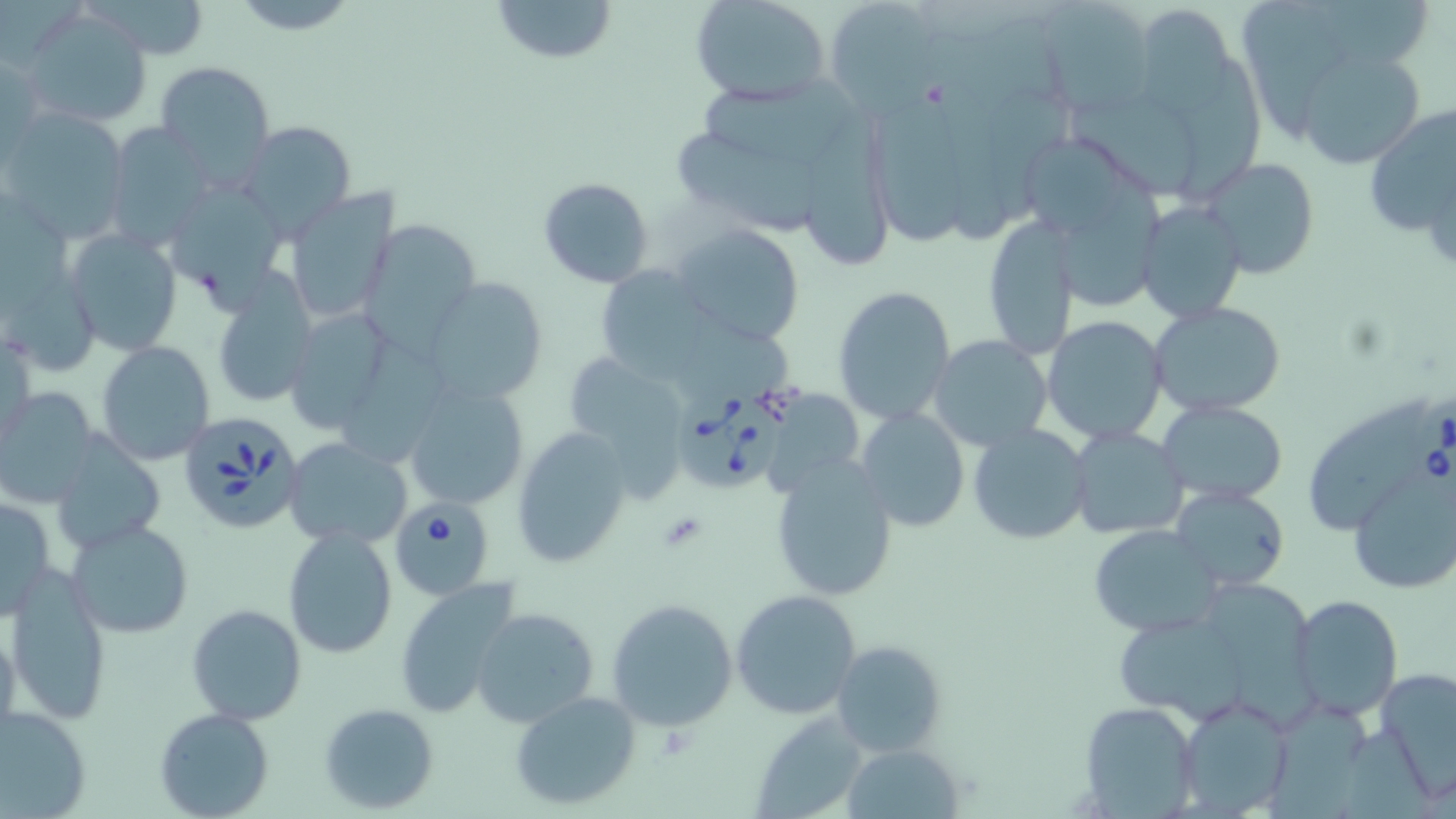

slide-level diagnosis = Babesia divergens
uninfected red blood cell locations = approximate bounding boxes as (x1,y1)-(x2,y2) corner pairs in pixels: (227,0)-(362,34), (490,0)-(619,65), (689,0)-(833,107), (823,0)-(947,114), (1036,0)-(1157,116), (1240,1)-(1365,145), (22,8)-(154,127), (1145,13)-(1235,123), (1296,47)-(1427,169), (1174,55)-(1270,209), (157,62)-(274,180), (704,75)-(859,159), (1071,96)-(1207,194), (873,99)-(972,252), (807,105)-(897,265), (1361,106)-(1456,242), (1,111)-(130,243), (238,121)-(356,237), (102,124)-(216,245), (673,127)-(811,231), (1197,157)-(1323,280), (1056,171)-(1166,305), (537,176)-(655,288), (175,186)-(287,311), (283,188)-(400,325), (1135,199)-(1247,323), (981,214)-(1082,360), (360,217)-(479,348), (670,222)-(807,345), (65,230)-(181,353), (597,267)-(720,386), (422,276)-(549,409), (211,282)-(319,410), (832,285)-(956,424), (1149,302)-(1288,419), (280,305)-(402,437), (1041,315)-(1169,444), (682,319)-(799,394), (928,335)-(1055,454), (352,338)-(447,464), (96,341)-(214,465), (576,358)-(698,501), (401,384)-(531,513), (0,387)-(99,509), (1157,399)-(1287,505), (1307,399)-(1434,535), (858,406)-(970,531), (967,422)-(1093,547), (511,426)-(630,568), (1068,427)-(1189,541), (49,434)-(166,556), (284,437)-(413,550), (768,455)-(899,599), (1345,466)-(1455,593), (1170,485)-(1290,592), (1,495)-(54,619), (67,519)-(194,638), (282,525)-(398,660), (1089,525)-(1224,635), (4,568)-(112,724), (394,577)-(522,719), (1215,579)-(1334,731), (730,589)-(862,719), (1287,594)-(1403,721), (607,598)-(738,731), (186,602)-(307,726), (471,608)-(600,729), (0,618)-(22,752), (1113,621)-(1244,716), (833,638)-(947,759), (1375,665)-(1456,797), (510,689)-(641,811), (1174,695)-(1294,818), (1079,701)-(1200,815), (319,702)-(440,814), (0,705)-(93,818), (1268,705)-(1371,819), (154,708)-(274,819), (750,712)-(871,817), (841,743)-(963,817)
Babesia divergens-infected red blood cell locations = approximate bounding boxes as (x1,y1)-(x2,y2) corner pairs in pixels: (679,381)-(786,491), (1405,392)-(1455,501), (177,411)-(304,535), (393,497)-(497,601)
modality = light microscopy
stain = May-Grünwald-Giemsa
platelet locations = approximate bounding boxes as (x1,y1)-(x2,y2) corner pairs in pixels: (659,512)-(710,552)
image size = 1456×819 pixels
preparation = thin blood smear
field of view = one of a larger specimen
magnification = 1000x